Assess the morphology of the red blood cells.
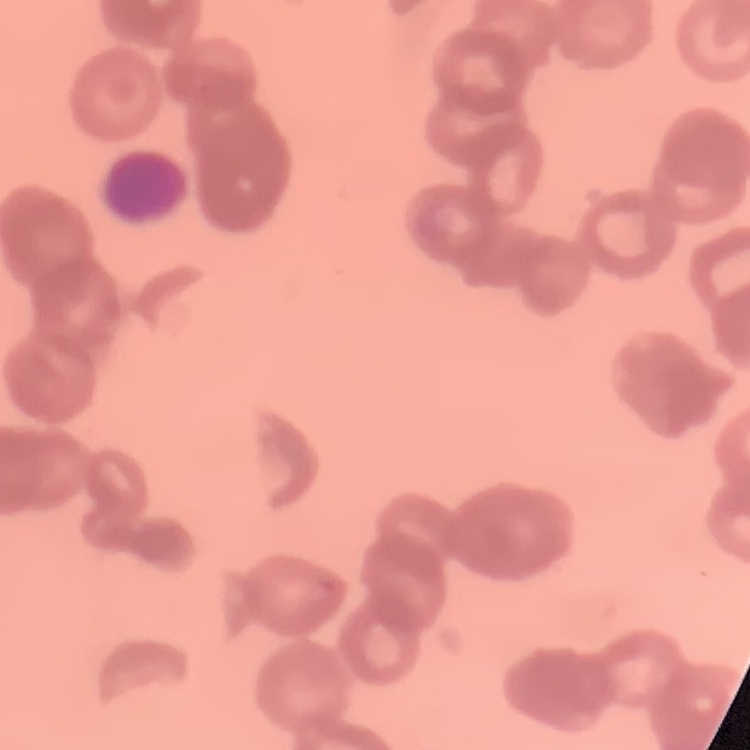

Rouleaux formation.

One tile cut from a larger photomicrograph. Field's or Giemsa stain. Thin blood film.